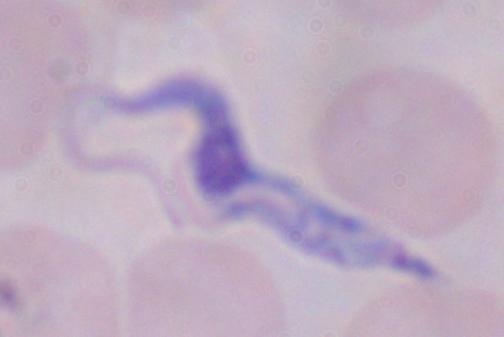
modality = micrograph
identification = trypanosome
magnification = 1000x